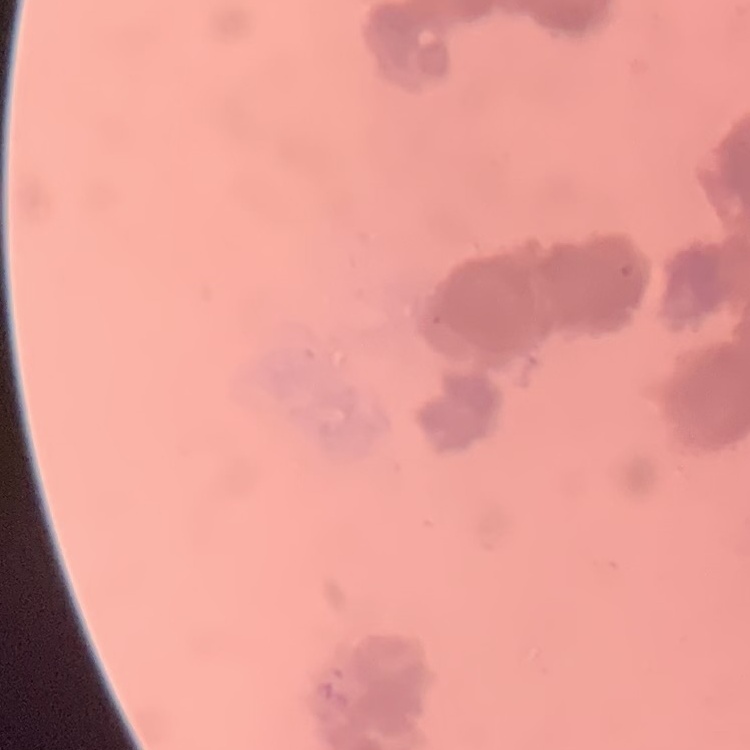

red blood cell morphology = rouleaux formation
image type = one tile cut from a larger photomicrograph
preparation = thin blood smear
stain = Field's or Giemsa